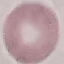
Summary:
  - Result: no malaria parasites seen
  - Image type: cell patch, automatically extracted from a larger field of view and resized to 64 × 64 pixels
  - Capture: smartphone camera at the microscope eyepiece
  - Preparation: thin smear
  - Stain: Giemsa